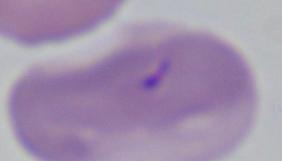 Captured at 1000x magnification. A Babesia parasite is seen. Photomicrograph.